Locate every leukocyte (white blood cell).
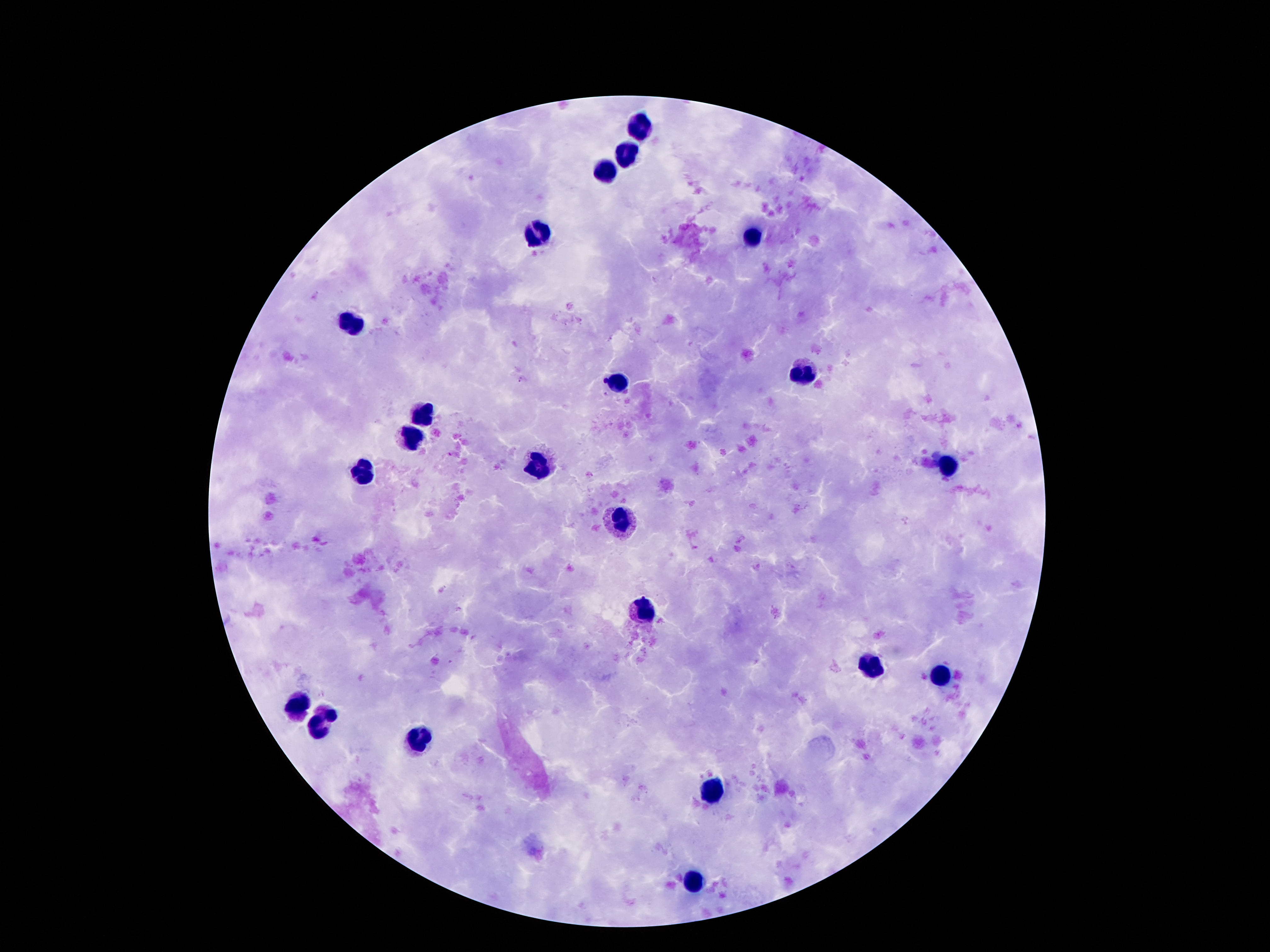

Approximate object centers, in pixels from the top-left corner.
Leukocytes: (x=639, y=127), (x=627, y=153), (x=604, y=172), (x=537, y=233), (x=754, y=238), (x=348, y=325), (x=800, y=369), (x=621, y=383), (x=423, y=412), (x=412, y=436), (x=537, y=467), (x=948, y=469), (x=366, y=472), (x=625, y=525), (x=645, y=614), (x=868, y=664), (x=938, y=675), (x=300, y=706), (x=321, y=724), (x=418, y=740), (x=714, y=793), (x=695, y=882).

{
  "patient_malaria_status": "uninfected",
  "magnification": "100x",
  "stain": "Giemsa",
  "preparation": "thick blood smear",
  "field_of_view": "single",
  "image_size": "1270×952 pixels",
  "capture": "smartphone camera through the microscope eyepiece"
}